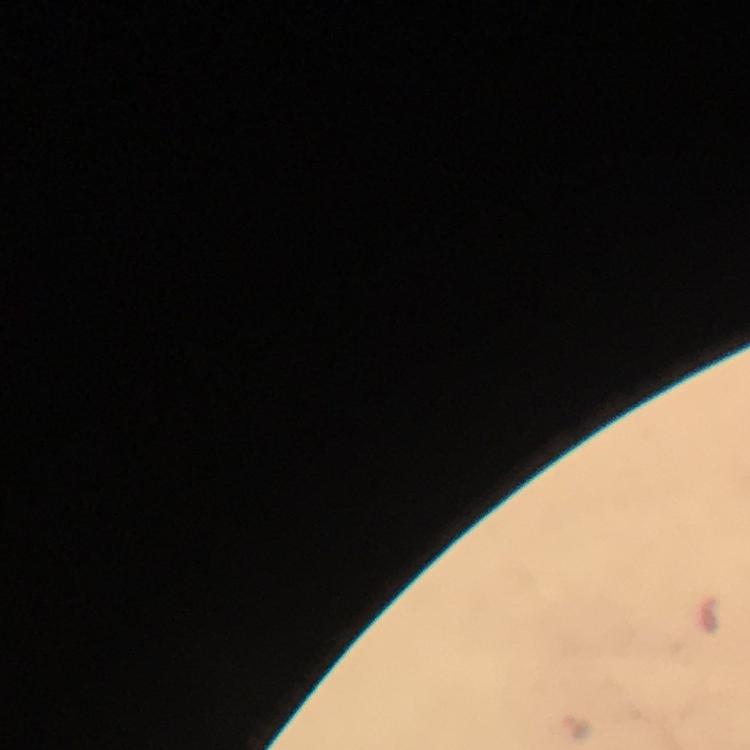
immersion oil = applied
malaria parasite locations = approximate centers as {x, y} in pixels: {580, 726}
cropped from = a single field of view
capture = smartphone mounted on the microscope
context = from a malaria diagnostic workup
image size = 750×750 pixels
preparation = thick blood film
stain = Giemsa
magnification = 100x